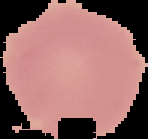

image size = 148×139 pixels
image type = cell region segmented out of the field of view; surrounding area masked to black
preparation = thin blood film
result = no malaria parasites seen